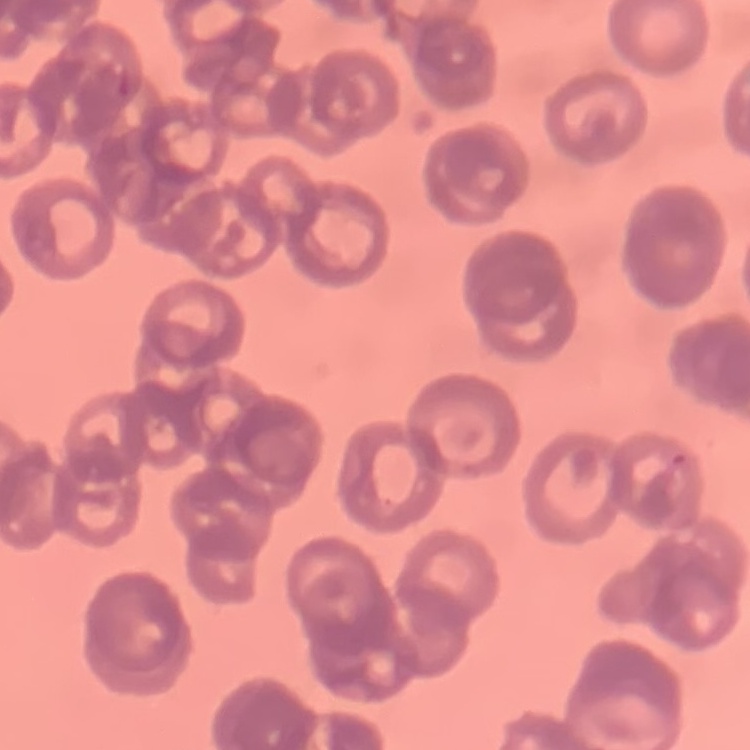

The erythrocytes exhibit rouleaux formation. Thin peripheral smear. Square crop of a larger photomicrograph. Field's or Giemsa stain.